Name the parasite shown.
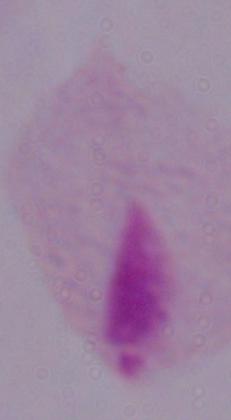
A trichomonad.

magnification: 1000x
modality: photomicrograph